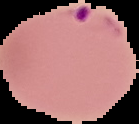
Summary:
  - Result: malaria parasites detected
  - Image type: segmented cell region with the area outside set to black
  - Preparation: thin blood smear
  - Image size: 139×124 pixels